Look for Plasmodium parasites.
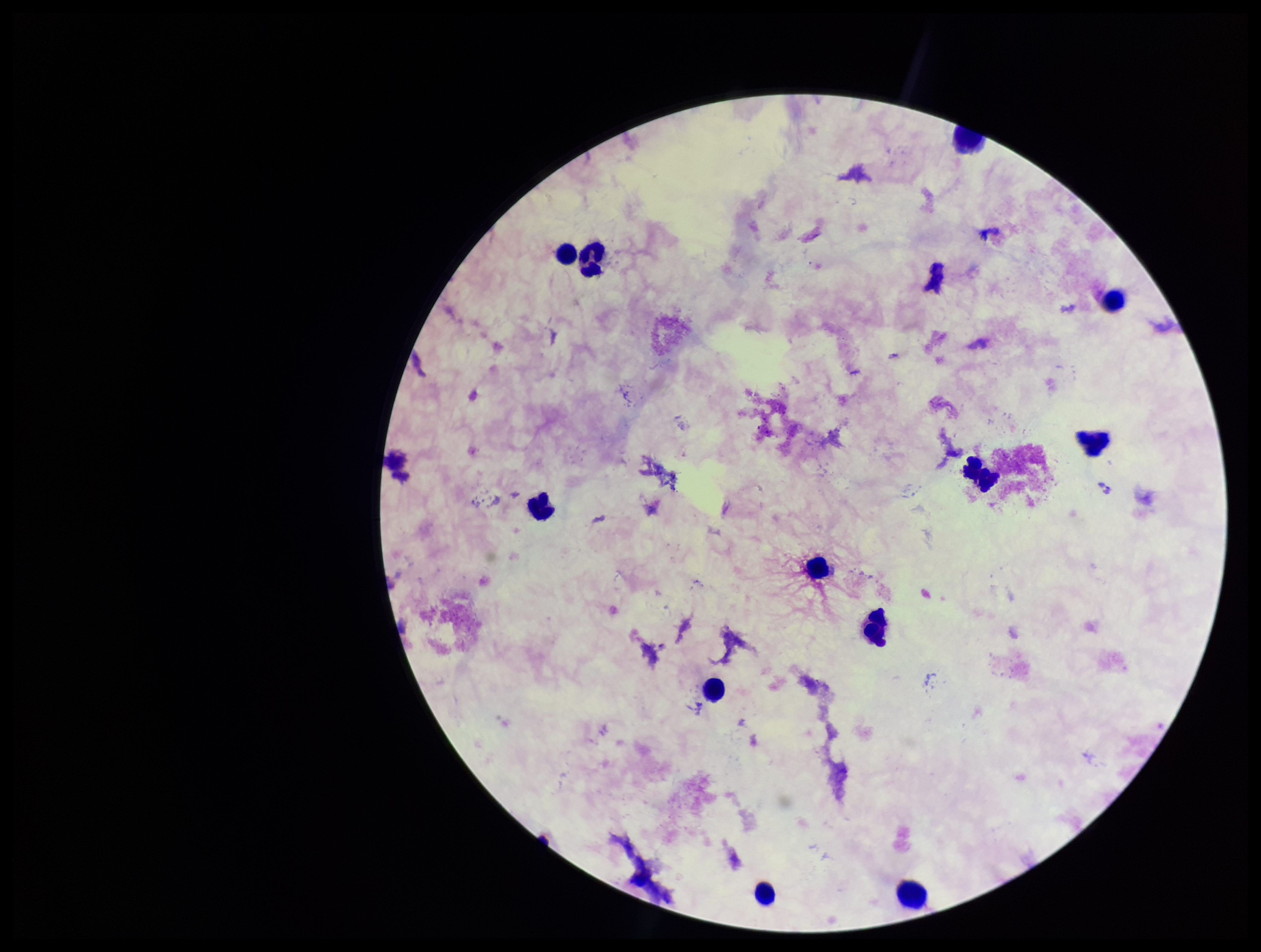

None identified.

Smartphone photograph taken through the eyepiece of a microscope. One field from this slide. Stained with Giemsa. Image is 1261×952 pixels. Leukocyte count: 12. Patient malaria status: negative. Parasite count: 0. Preparation: thick smear.